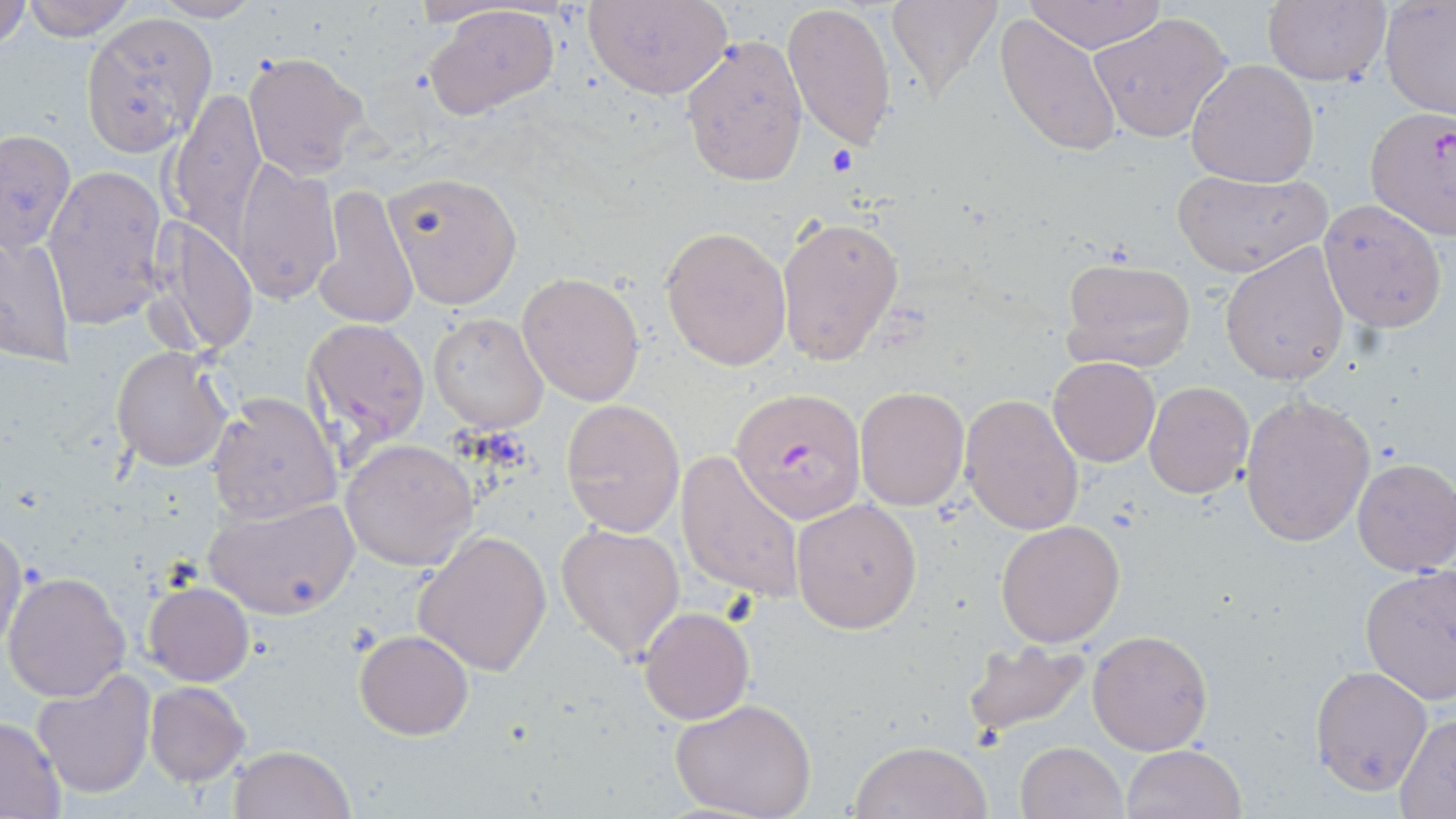

Approximate bounding boxes as (x1,y1)-(x2,y2) corner pairs in pixels. Uninfected red blood cell locations: (0,0)-(30,53), (19,0)-(138,40), (584,0)-(734,100), (884,0)-(1005,101), (1020,0)-(1168,53), (1261,0)-(1392,89), (1380,0)-(1456,120), (149,1)-(260,23), (783,1)-(897,152), (424,5)-(560,120), (81,11)-(218,153), (1088,12)-(1235,144), (993,13)-(1124,158), (680,33)-(809,188), (243,53)-(369,177), (1186,58)-(1319,188), (168,87)-(268,241), (1,126)-(77,258), (230,159)-(341,306), (42,163)-(170,330), (1172,170)-(1330,275), (386,171)-(522,311), (313,183)-(419,328), (1319,199)-(1448,333), (777,214)-(905,369), (155,219)-(256,357), (658,225)-(791,371), (1,233)-(74,368), (1220,241)-(1350,385), (1058,255)-(1200,375), (518,272)-(645,405), (427,312)-(548,433), (303,317)-(428,452), (110,346)-(232,472), (1047,356)-(1161,467), (1143,382)-(1254,500), (855,386)-(969,510), (208,392)-(340,524), (960,393)-(1086,536), (1239,394)-(1377,548), (561,398)-(686,537), (340,439)-(477,571), (677,449)-(806,604), (1352,459)-(1456,576), (203,497)-(360,619), (792,497)-(923,634), (995,519)-(1126,649), (1,520)-(29,656), (555,521)-(685,663), (414,529)-(552,676), (1360,566)-(1456,704), (2,570)-(131,703), (143,581)-(254,686), (639,606)-(755,726), (1087,629)-(1215,754), (354,630)-(474,740), (961,635)-(1094,739), (1309,664)-(1434,796), (31,671)-(156,800), (145,681)-(249,785), (669,698)-(818,819), (1393,713)-(1456,814), (0,716)-(67,817), (848,740)-(991,819), (1015,740)-(1127,819), (1123,744)-(1246,819), (228,745)-(355,819). Platelet locations: (827,146)-(858,175). Plasmodium falciparum-infected red blood cell locations: (1363,105)-(1456,238), (727,387)-(868,524). Slide-level diagnosis: Plasmodium falciparum. Optical microscopy. One field of a larger specimen. 1000x magnification. Image is 1456×819 pixels. May-Grünwald-Giemsa-stained preparation. Thin blood film.